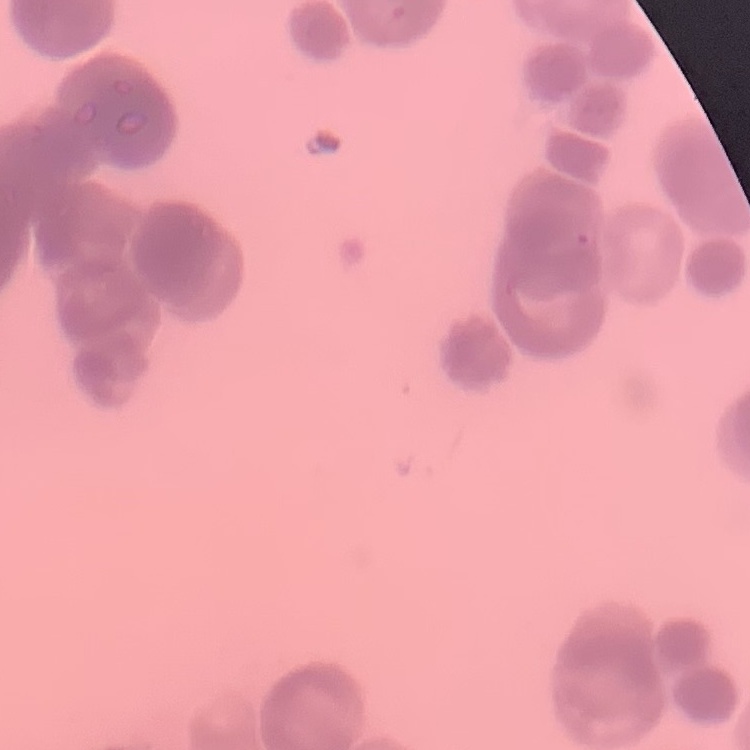
erythrocyte morphology = rouleaux formation
preparation = thin peripheral smear
stain = Field's or Giemsa
image type = one tile cut from a larger photomicrograph